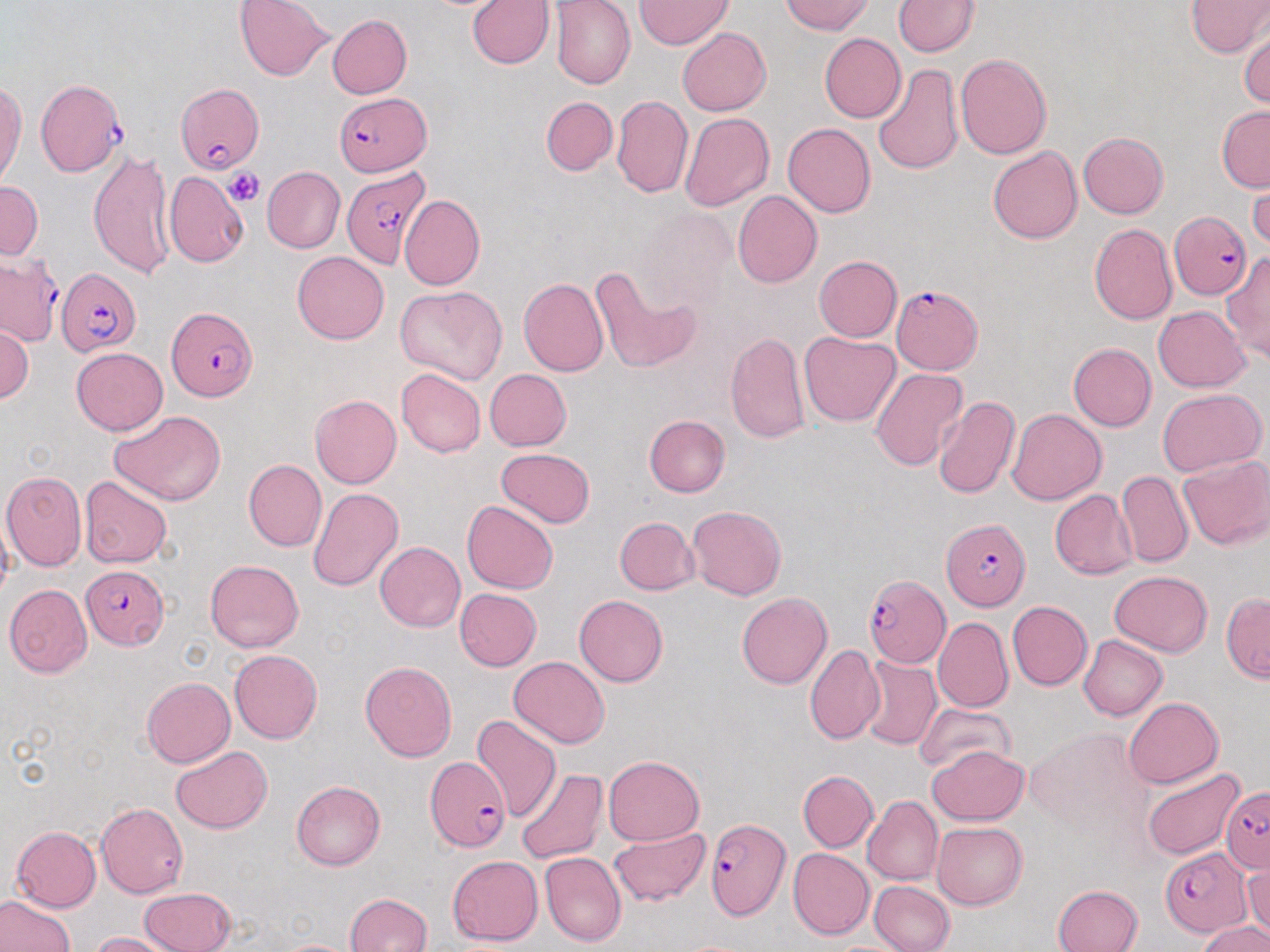 Approximate bounding boxes as named x1/y1/x2/y2 corners in pixels. Uninfected red blood cell locations: (x1=234, y1=0, x2=333, y2=81), (x1=549, y1=0, x2=635, y2=89), (x1=634, y1=0, x2=734, y2=49), (x1=781, y1=0, x2=874, y2=35), (x1=1184, y1=0, x2=1270, y2=56), (x1=467, y1=1, x2=554, y2=69), (x1=893, y1=1, x2=980, y2=57), (x1=328, y1=15, x2=412, y2=98), (x1=677, y1=27, x2=772, y2=115), (x1=1239, y1=28, x2=1269, y2=109), (x1=818, y1=33, x2=906, y2=123), (x1=955, y1=54, x2=1052, y2=159), (x1=871, y1=62, x2=964, y2=175), (x1=0, y1=81, x2=25, y2=190), (x1=612, y1=95, x2=693, y2=198), (x1=541, y1=96, x2=617, y2=176), (x1=1216, y1=105, x2=1270, y2=191), (x1=678, y1=113, x2=774, y2=213), (x1=783, y1=123, x2=876, y2=217), (x1=1078, y1=131, x2=1168, y2=218), (x1=988, y1=145, x2=1083, y2=244), (x1=89, y1=149, x2=177, y2=281), (x1=263, y1=167, x2=346, y2=253), (x1=163, y1=171, x2=249, y2=267), (x1=1247, y1=175, x2=1269, y2=254), (x1=0, y1=181, x2=43, y2=260), (x1=733, y1=190, x2=823, y2=288), (x1=399, y1=194, x2=485, y2=290), (x1=634, y1=210, x2=737, y2=314), (x1=1089, y1=223, x2=1177, y2=325), (x1=292, y1=251, x2=389, y2=344), (x1=1220, y1=253, x2=1270, y2=362), (x1=815, y1=255, x2=902, y2=341), (x1=590, y1=264, x2=701, y2=374), (x1=518, y1=278, x2=608, y2=377), (x1=396, y1=286, x2=508, y2=386), (x1=1153, y1=306, x2=1252, y2=391), (x1=0, y1=321, x2=33, y2=404), (x1=799, y1=331, x2=900, y2=426), (x1=725, y1=332, x2=810, y2=442), (x1=1068, y1=343, x2=1156, y2=430), (x1=71, y1=347, x2=168, y2=436), (x1=870, y1=367, x2=968, y2=472), (x1=396, y1=368, x2=486, y2=456), (x1=484, y1=368, x2=571, y2=450), (x1=1158, y1=389, x2=1267, y2=476), (x1=310, y1=394, x2=401, y2=489), (x1=933, y1=397, x2=1020, y2=500), (x1=1006, y1=408, x2=1107, y2=505), (x1=110, y1=410, x2=227, y2=504), (x1=643, y1=415, x2=730, y2=497), (x1=496, y1=448, x2=596, y2=527), (x1=1177, y1=456, x2=1270, y2=551), (x1=243, y1=459, x2=326, y2=551), (x1=1, y1=470, x2=87, y2=571), (x1=1116, y1=470, x2=1193, y2=568), (x1=80, y1=476, x2=172, y2=568), (x1=308, y1=487, x2=404, y2=591), (x1=1050, y1=490, x2=1138, y2=580), (x1=463, y1=500, x2=558, y2=594), (x1=687, y1=505, x2=787, y2=600), (x1=1, y1=508, x2=14, y2=603), (x1=614, y1=516, x2=699, y2=595), (x1=374, y1=541, x2=465, y2=632), (x1=205, y1=559, x2=303, y2=653), (x1=1109, y1=571, x2=1214, y2=656), (x1=4, y1=584, x2=92, y2=678), (x1=454, y1=588, x2=542, y2=671), (x1=737, y1=592, x2=833, y2=688), (x1=1221, y1=593, x2=1270, y2=682), (x1=575, y1=594, x2=668, y2=687), (x1=1008, y1=601, x2=1092, y2=690), (x1=932, y1=616, x2=1013, y2=712), (x1=1077, y1=635, x2=1167, y2=721), (x1=805, y1=644, x2=885, y2=745), (x1=229, y1=649, x2=321, y2=744), (x1=509, y1=656, x2=610, y2=748), (x1=858, y1=656, x2=941, y2=751), (x1=360, y1=660, x2=457, y2=762), (x1=141, y1=677, x2=234, y2=767), (x1=1122, y1=697, x2=1224, y2=788), (x1=914, y1=703, x2=1014, y2=778), (x1=472, y1=714, x2=561, y2=823), (x1=928, y1=745, x2=1029, y2=826), (x1=171, y1=746, x2=273, y2=833), (x1=603, y1=755, x2=705, y2=845), (x1=1140, y1=766, x2=1245, y2=860), (x1=516, y1=767, x2=608, y2=865), (x1=798, y1=770, x2=878, y2=852), (x1=292, y1=779, x2=385, y2=869), (x1=863, y1=796, x2=943, y2=886), (x1=95, y1=803, x2=188, y2=898), (x1=932, y1=821, x2=1028, y2=910), (x1=11, y1=826, x2=102, y2=912), (x1=609, y1=827, x2=710, y2=909), (x1=788, y1=848, x2=874, y2=940), (x1=540, y1=852, x2=626, y2=947), (x1=448, y1=855, x2=543, y2=946), (x1=1244, y1=860, x2=1270, y2=942), (x1=868, y1=881, x2=954, y2=952), (x1=1053, y1=884, x2=1144, y2=952), (x1=138, y1=886, x2=236, y2=952), (x1=0, y1=892, x2=75, y2=952), (x1=344, y1=892, x2=433, y2=952), (x1=1198, y1=921, x2=1270, y2=952), (x1=90, y1=932, x2=179, y2=952), (x1=272, y1=938, x2=360, y2=951). Plasmodium falciparum-infected red blood cell locations: (x1=36, y1=78, x2=125, y2=177), (x1=176, y1=83, x2=264, y2=174), (x1=333, y1=92, x2=432, y2=174), (x1=342, y1=169, x2=431, y2=267), (x1=1167, y1=212, x2=1252, y2=303), (x1=0, y1=252, x2=62, y2=347), (x1=57, y1=266, x2=142, y2=360), (x1=890, y1=285, x2=981, y2=374), (x1=166, y1=307, x2=257, y2=402), (x1=942, y1=518, x2=1031, y2=611), (x1=81, y1=566, x2=169, y2=649), (x1=864, y1=574, x2=950, y2=666), (x1=424, y1=756, x2=510, y2=853), (x1=1220, y1=785, x2=1270, y2=873), (x1=706, y1=818, x2=790, y2=920), (x1=1161, y1=849, x2=1251, y2=936). Platelet locations: (x1=225, y1=167, x2=263, y2=206). Slide-level diagnosis: Plasmodium falciparum. Image is 1270×952 pixels. Thin blood smear. Light microscopy. Single field of view. 1000x magnification. May-Grünwald-Giemsa-stained preparation.